Assess for malaria.
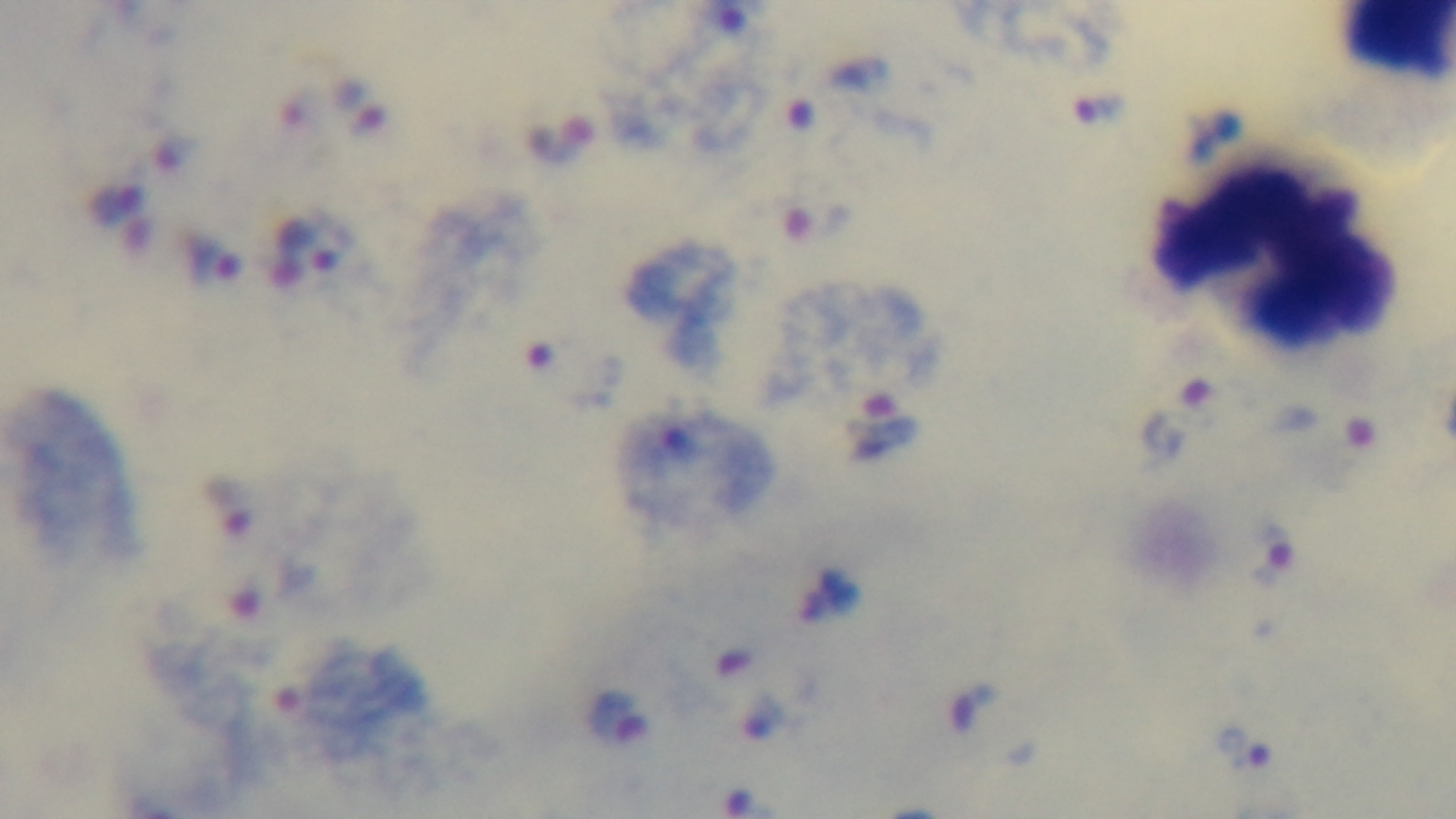
Infected.

field_of_view: one from the slide
stain: Giemsa
preparation: thick blood film
objective: 100x oil immersion
modality: light microscopy
capture: mounted 4K digital camera